Locate every blood parasite and identify its species.
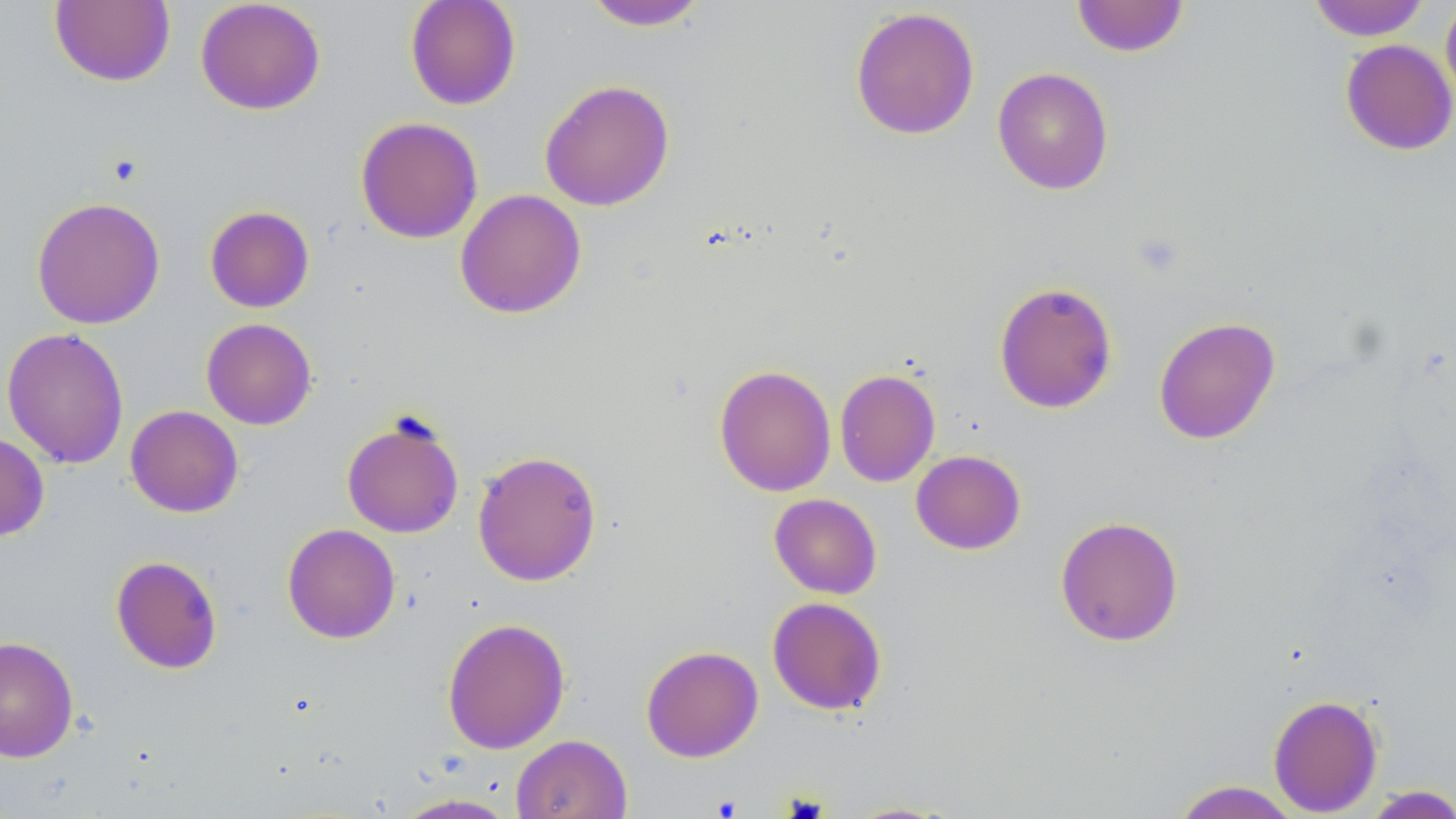

No blood parasites seen.

Summary:
  - Coordinate format: approximate bounding boxes as named x1/y1/x2/y2 corners in pixels
  - Uninfected red blood cell locations: (x1=195, y1=0, x2=326, y2=115), (x1=405, y1=0, x2=521, y2=110), (x1=1071, y1=0, x2=1190, y2=57), (x1=1306, y1=0, x2=1430, y2=41), (x1=49, y1=1, x2=175, y2=87), (x1=583, y1=1, x2=710, y2=31), (x1=1441, y1=1, x2=1456, y2=110), (x1=850, y1=6, x2=980, y2=140), (x1=1340, y1=39, x2=1456, y2=155), (x1=992, y1=67, x2=1114, y2=195), (x1=539, y1=79, x2=675, y2=211), (x1=355, y1=116, x2=483, y2=244), (x1=455, y1=189, x2=587, y2=319), (x1=32, y1=196, x2=165, y2=329), (x1=204, y1=205, x2=314, y2=312), (x1=994, y1=281, x2=1118, y2=414), (x1=1153, y1=316, x2=1280, y2=445), (x1=201, y1=318, x2=317, y2=430), (x1=2, y1=326, x2=129, y2=468), (x1=714, y1=364, x2=836, y2=497), (x1=835, y1=368, x2=941, y2=487), (x1=125, y1=405, x2=243, y2=517), (x1=341, y1=412, x2=465, y2=540), (x1=0, y1=431, x2=50, y2=542), (x1=472, y1=450, x2=602, y2=586), (x1=911, y1=450, x2=1026, y2=555), (x1=769, y1=493, x2=882, y2=598), (x1=1055, y1=515, x2=1184, y2=646), (x1=282, y1=523, x2=400, y2=643), (x1=110, y1=555, x2=223, y2=674), (x1=767, y1=596, x2=887, y2=715), (x1=442, y1=617, x2=570, y2=754), (x1=0, y1=635, x2=79, y2=763), (x1=641, y1=645, x2=763, y2=762), (x1=1268, y1=694, x2=1384, y2=816), (x1=511, y1=734, x2=632, y2=819), (x1=1171, y1=781, x2=1302, y2=819), (x1=1359, y1=785, x2=1456, y2=819), (x1=393, y1=792, x2=518, y2=818), (x1=840, y1=800, x2=961, y2=818)
  - Slide-level diagnosis: no evidence of blood parasites
  - Stain: May-Grünwald-Giemsa
  - Image size: 1456×819 pixels
  - Magnification: 1000x
  - Field of view: one of a larger specimen
  - Preparation: thin blood smear
  - Modality: optical microscopy